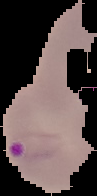

{
  "malaria_status": "parasitized",
  "preparation": "thin blood film",
  "image_type": "cell region segmented out of the field of view; surrounding area masked to black",
  "image_size": "97×196 pixels"
}